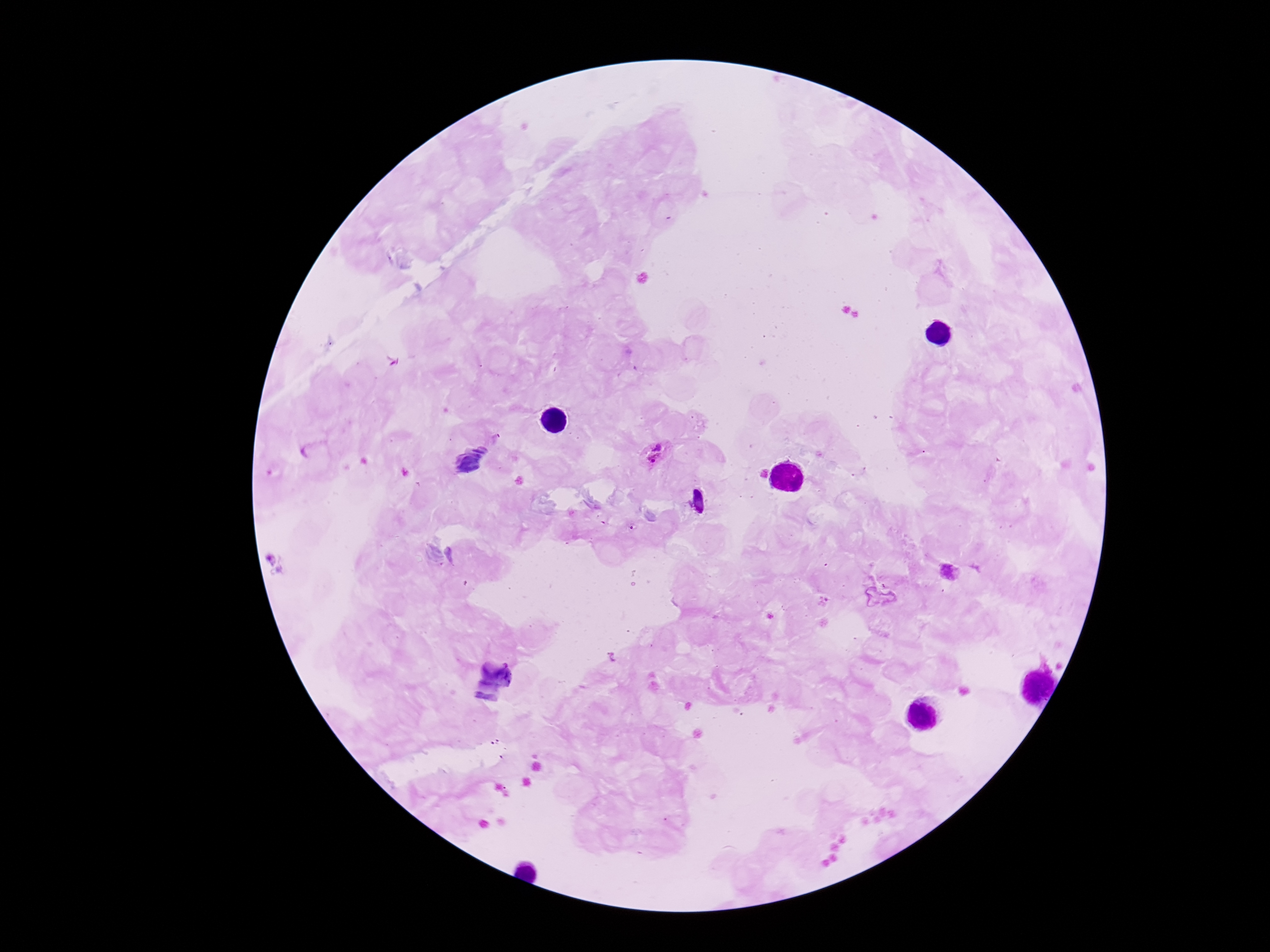

image size = 1270×952 pixels
stain = Giemsa
field of view = single
preparation = thick blood smear
Plasmodium parasite locations = approximate object centers, in pixels from the top-left corner: (x=654, y=453), (x=950, y=572)
magnification = 100x
patient malaria status = positive
capture = smartphone camera through the microscope eyepiece